Classify this cell by malaria status.
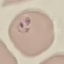
Parasitized.

Summary:
  - Stain: Giemsa
  - Preparation: thin smear
  - Image type: cell patch, automatically extracted from a larger field of view and resized to 64 × 64 pixels
  - Capture: smartphone through the microscope eyepiece